Name the parasite shown.
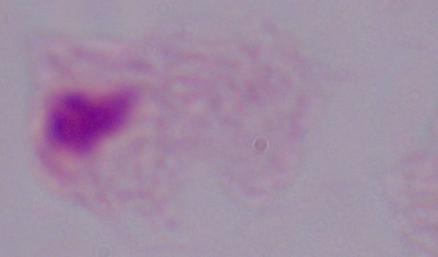
This is a trichomonad.

magnification = 1000x
modality = micrograph